Outline each Plasmodium ovale-infected red blood cell.
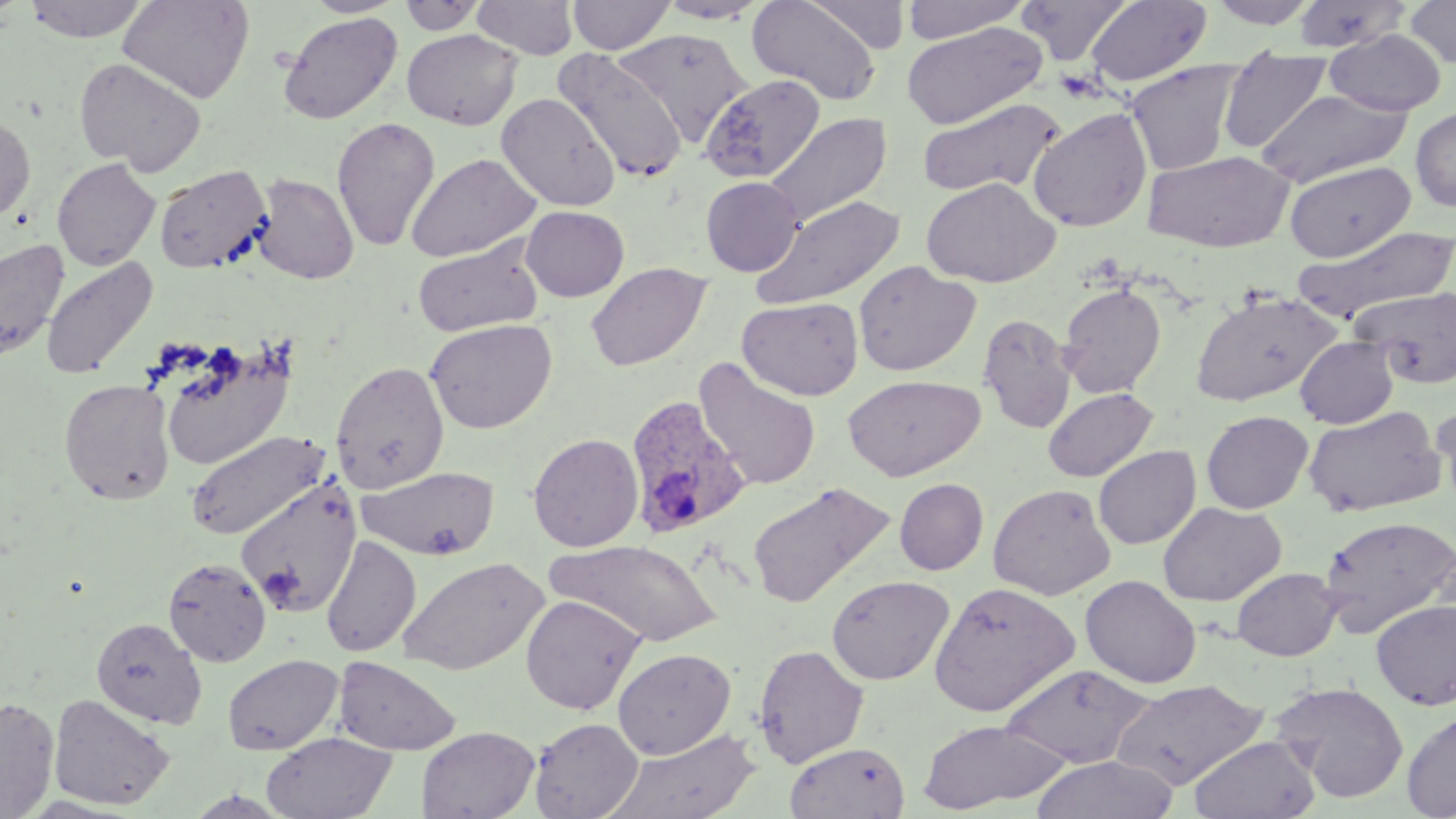

Approximate bounding boxes as named x1/y1/x2/y2 corners in pixels.
Plasmodium ovale-infected red blood cells: (x1=624, y1=395, x2=751, y2=538).

Uninfected red blood cell locations: (x1=23, y1=0, x2=150, y2=42), (x1=118, y1=0, x2=254, y2=104), (x1=304, y1=0, x2=407, y2=18), (x1=472, y1=0, x2=578, y2=59), (x1=567, y1=0, x2=675, y2=55), (x1=655, y1=0, x2=770, y2=23), (x1=748, y1=0, x2=882, y2=106), (x1=804, y1=0, x2=909, y2=53), (x1=899, y1=0, x2=1031, y2=43), (x1=1017, y1=0, x2=1131, y2=65), (x1=1086, y1=0, x2=1212, y2=88), (x1=1207, y1=0, x2=1320, y2=28), (x1=1291, y1=0, x2=1411, y2=54), (x1=1404, y1=0, x2=1456, y2=69), (x1=399, y1=1, x2=487, y2=35), (x1=277, y1=12, x2=403, y2=125), (x1=902, y1=22, x2=1047, y2=129), (x1=402, y1=28, x2=522, y2=129), (x1=616, y1=28, x2=751, y2=144), (x1=1324, y1=29, x2=1446, y2=116), (x1=554, y1=50, x2=689, y2=181), (x1=74, y1=56, x2=206, y2=176), (x1=1218, y1=57, x2=1332, y2=153), (x1=1125, y1=61, x2=1244, y2=176), (x1=700, y1=73, x2=826, y2=184), (x1=1254, y1=88, x2=1414, y2=187), (x1=495, y1=93, x2=620, y2=212), (x1=916, y1=97, x2=1066, y2=199), (x1=1027, y1=106, x2=1153, y2=233), (x1=1411, y1=107, x2=1456, y2=212), (x1=0, y1=113, x2=36, y2=222), (x1=765, y1=113, x2=892, y2=229), (x1=331, y1=116, x2=441, y2=254), (x1=1143, y1=150, x2=1294, y2=252), (x1=406, y1=153, x2=541, y2=262), (x1=52, y1=158, x2=160, y2=271), (x1=1284, y1=160, x2=1415, y2=262), (x1=154, y1=164, x2=272, y2=275), (x1=251, y1=173, x2=359, y2=284), (x1=700, y1=176, x2=803, y2=276), (x1=920, y1=178, x2=1059, y2=288), (x1=753, y1=194, x2=905, y2=311), (x1=520, y1=205, x2=629, y2=302), (x1=1296, y1=226, x2=1453, y2=321), (x1=0, y1=237, x2=70, y2=364), (x1=413, y1=241, x2=542, y2=336), (x1=40, y1=256, x2=158, y2=380), (x1=853, y1=261, x2=980, y2=377), (x1=585, y1=262, x2=712, y2=371), (x1=1058, y1=282, x2=1167, y2=399), (x1=1352, y1=286, x2=1456, y2=388), (x1=1190, y1=289, x2=1340, y2=406), (x1=737, y1=297, x2=863, y2=401), (x1=977, y1=313, x2=1077, y2=433), (x1=424, y1=319, x2=558, y2=434), (x1=1295, y1=336, x2=1399, y2=428), (x1=157, y1=342, x2=295, y2=471), (x1=695, y1=359, x2=821, y2=492), (x1=331, y1=360, x2=450, y2=494), (x1=842, y1=374, x2=985, y2=481), (x1=59, y1=378, x2=176, y2=505), (x1=1043, y1=388, x2=1158, y2=483), (x1=1432, y1=398, x2=1456, y2=514), (x1=1303, y1=405, x2=1447, y2=518), (x1=1201, y1=410, x2=1314, y2=514), (x1=184, y1=430, x2=331, y2=542), (x1=528, y1=433, x2=644, y2=552), (x1=1093, y1=445, x2=1201, y2=550), (x1=357, y1=466, x2=501, y2=561), (x1=235, y1=477, x2=361, y2=618), (x1=895, y1=478, x2=988, y2=575), (x1=747, y1=481, x2=894, y2=609), (x1=988, y1=483, x2=1116, y2=600), (x1=1158, y1=501, x2=1286, y2=606), (x1=1318, y1=515, x2=1455, y2=637), (x1=320, y1=535, x2=421, y2=657), (x1=548, y1=538, x2=722, y2=647), (x1=398, y1=556, x2=549, y2=676), (x1=163, y1=557, x2=271, y2=667), (x1=1232, y1=568, x2=1342, y2=661), (x1=826, y1=575, x2=954, y2=686), (x1=1080, y1=575, x2=1201, y2=688), (x1=929, y1=581, x2=1081, y2=717), (x1=520, y1=594, x2=644, y2=714), (x1=1371, y1=599, x2=1456, y2=710), (x1=91, y1=616, x2=208, y2=730), (x1=752, y1=643, x2=869, y2=768), (x1=613, y1=648, x2=736, y2=759), (x1=222, y1=653, x2=343, y2=755), (x1=333, y1=656, x2=461, y2=755), (x1=999, y1=663, x2=1156, y2=770), (x1=1109, y1=678, x2=1268, y2=790), (x1=1271, y1=680, x2=1409, y2=803), (x1=48, y1=693, x2=175, y2=811), (x1=0, y1=696, x2=59, y2=817), (x1=1402, y1=710, x2=1456, y2=818), (x1=529, y1=717, x2=643, y2=819), (x1=917, y1=719, x2=1071, y2=813), (x1=416, y1=725, x2=540, y2=819), (x1=604, y1=728, x2=761, y2=819), (x1=261, y1=732, x2=397, y2=819), (x1=1189, y1=734, x2=1321, y2=818), (x1=785, y1=741, x2=910, y2=819), (x1=1029, y1=755, x2=1178, y2=818). Slide-level diagnosis: Plasmodium ovale. May-Grünwald-Giemsa stain. Image is 1456×819 pixels. Light microscopy. 1000x magnification. Single field of view. Thin blood smear.